Locate and identify every blood parasite.
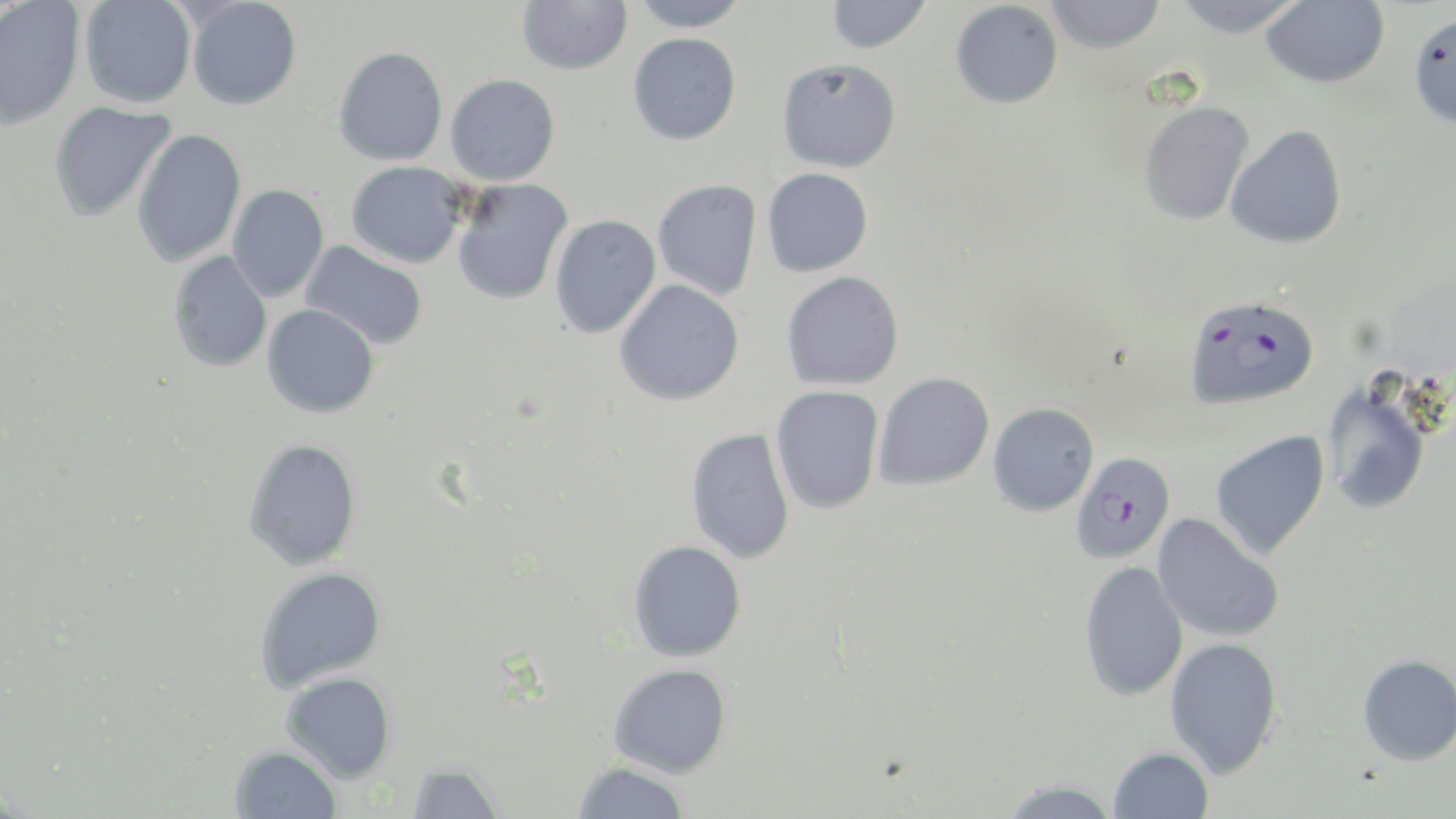

Approximate bounding boxes as (x1,y1)-(x2,y2) corner pairs in pixels.
Plasmodium falciparum-infected red blood cells: (1182,294)-(1319,410), (1070,451)-(1175,564).
No Plasmodium ovale, Plasmodium malariae, Plasmodium vivax, Babesia divergens, or Trypanosoma brucei observed.

Uninfected red blood cell locations: (186,0)-(302,110), (517,0)-(632,75), (629,0)-(750,32), (825,0)-(931,53), (1044,0)-(1167,53), (1173,0)-(1305,37), (0,1)-(85,129), (79,1)-(197,109), (950,1)-(1063,109), (1259,1)-(1390,88), (1408,11)-(1456,128), (628,33)-(741,145), (333,46)-(448,166), (777,57)-(901,172), (445,74)-(560,186), (1138,100)-(1255,226), (47,101)-(176,224), (1225,125)-(1347,249), (131,129)-(246,267), (346,161)-(467,268), (762,167)-(874,277), (451,178)-(574,305), (652,179)-(762,301), (227,184)-(329,302), (549,214)-(661,339), (300,241)-(428,350), (167,251)-(273,372), (782,271)-(904,390), (614,280)-(745,406), (262,304)-(379,418), (873,372)-(995,490), (1320,384)-(1433,514), (770,385)-(885,515), (987,403)-(1099,516), (685,427)-(796,564), (1210,430)-(1330,560), (242,437)-(362,571), (1153,514)-(1286,643), (628,540)-(747,662), (1078,561)-(1189,702), (254,566)-(387,692), (1164,636)-(1284,777), (1357,653)-(1456,766), (608,663)-(731,777), (281,671)-(397,783), (230,745)-(342,818), (1108,745)-(1214,818), (572,761)-(690,819), (404,762)-(506,818), (996,778)-(1122,819). Slide-level diagnosis: Plasmodium falciparum. Image is 1456×819 pixels. Single field of view. Light microscopy. Thin blood smear. 1000x magnification. May-Grünwald-Giemsa-stained preparation.